Report the malaria status of this cell.
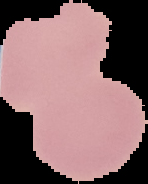
Uninfected.

image size = 148×184 pixels
preparation = thin blood film
image type = segmented cell region with the area outside set to black